Identify the preparation type.
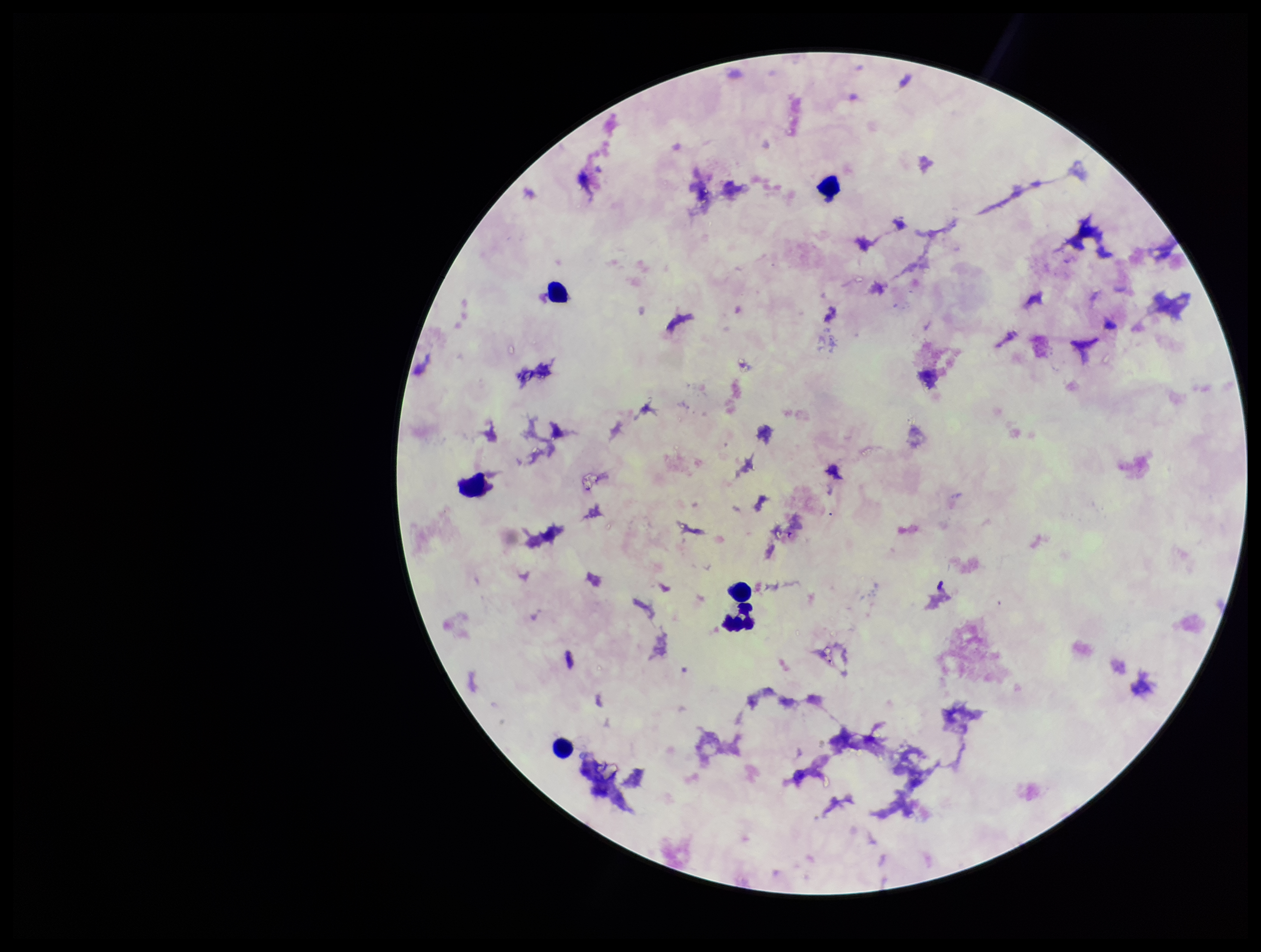
It is a thick blood smear.

Summary:
  - Image size: 1261×952 pixels
  - Capture: smartphone photograph through the microscope eyepiece
  - Field of view: single
  - Leukocyte count: 6
  - Parasite count: 0
  - Plasmodium parasites: none identified
  - Patient malaria status: negative
  - Stain: Giemsa